Name the parasite shown.
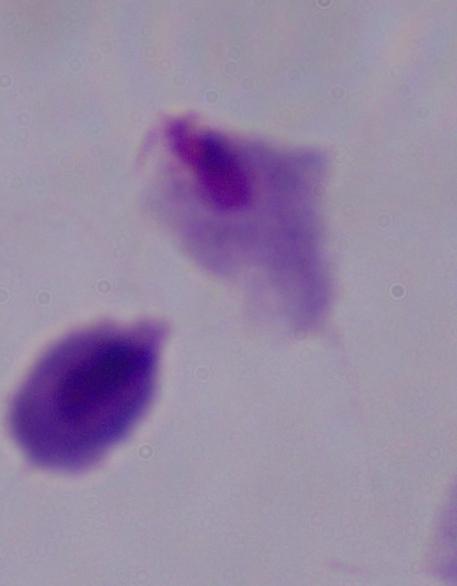
This is a trichomonad.

magnification = 1000x
modality = micrograph